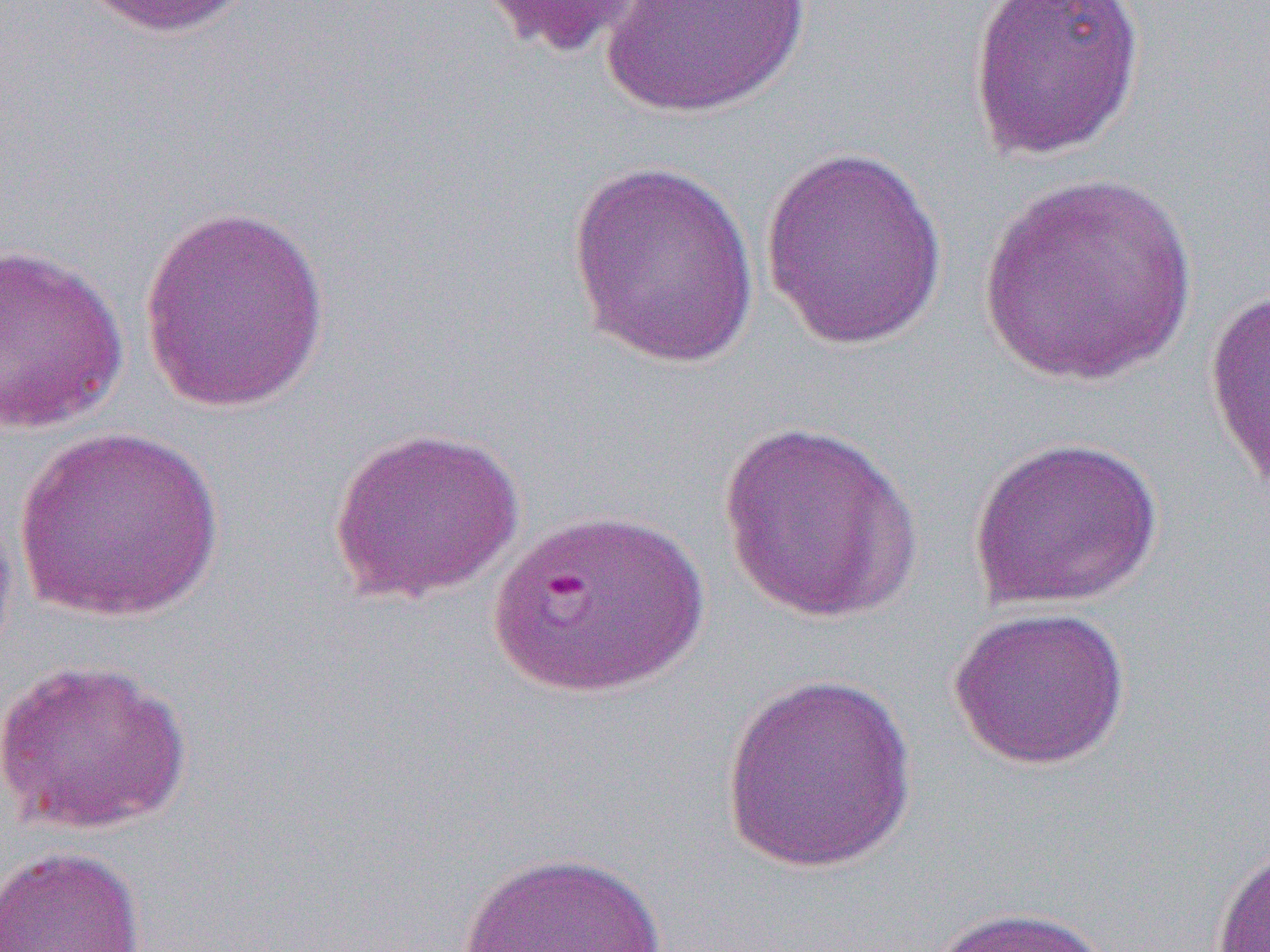

Summary:
  - Coordinate format: approximate bounding boxes as [x1, y1, x2, y2] in pixels
  - Uninfected red blood cell locations: [75, 0, 255, 39], [475, 0, 657, 60], [600, 0, 813, 119], [966, 0, 1146, 161], [758, 144, 949, 350], [565, 161, 761, 368], [974, 171, 1201, 387], [139, 204, 332, 415], [0, 242, 129, 435], [1203, 285, 1270, 496], [716, 421, 923, 623], [12, 425, 226, 622], [327, 425, 525, 605], [967, 435, 1165, 611], [0, 490, 20, 674], [947, 604, 1131, 771], [0, 657, 195, 834], [719, 672, 918, 874], [1210, 839, 1270, 952], [0, 845, 146, 952], [451, 849, 680, 952], [926, 904, 1114, 952]
  - Slide-level diagnosis: Plasmodium falciparum
  - Preparation: thin blood film
  - Modality: light microscopy
  - Magnification: 1000x
  - Field of view: single
  - Image size: 1270×952 pixels